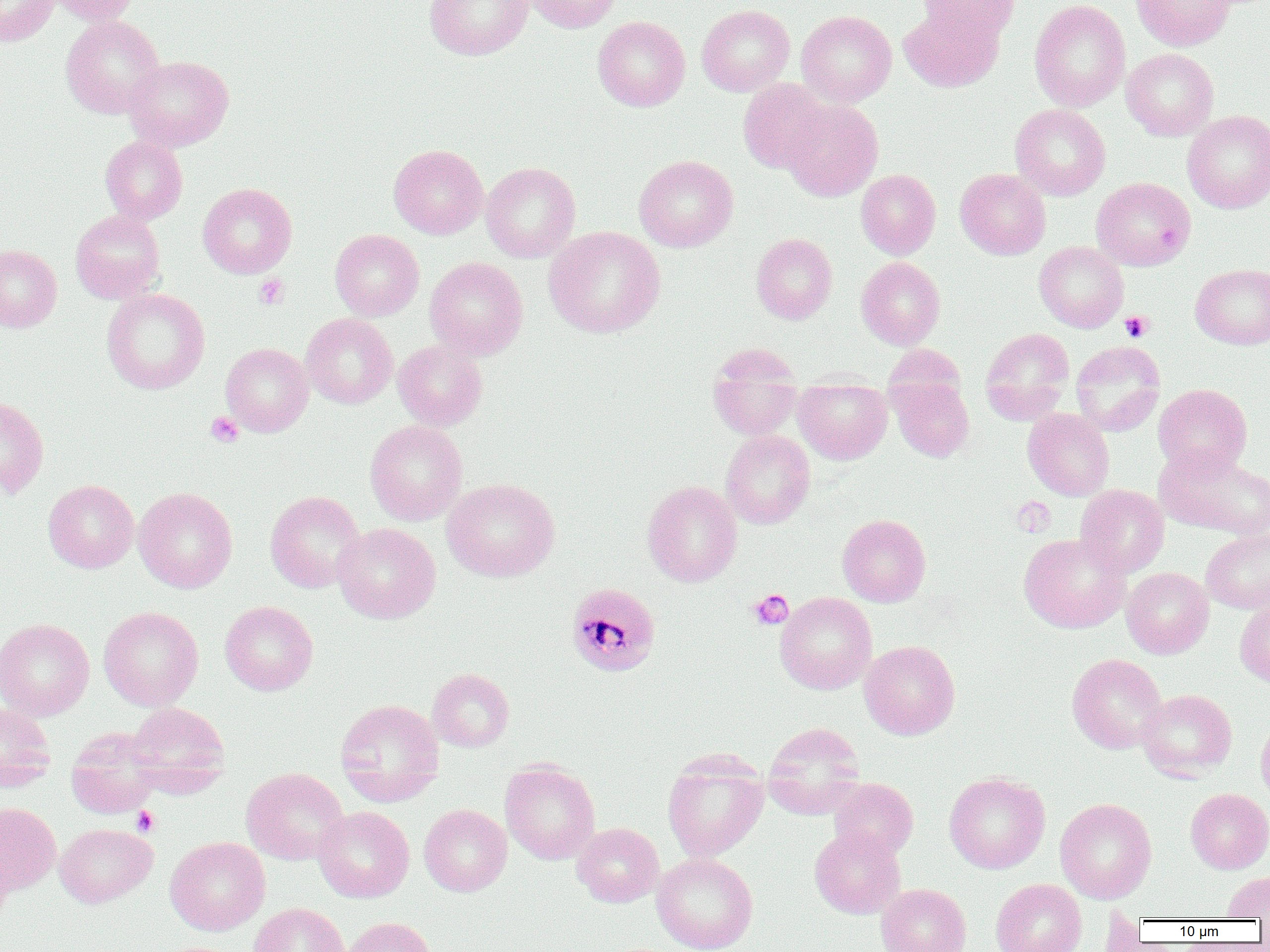

slide_level_diagnosis: Plasmodium malariae
preparation: thin blood smear
platelet_locations: 'approximate bounding boxes as (x1,y1)-(x2,y2) corner pairs in pixels: (254,274)-(289,309), (1120,311)-(1153,342), (205,412)-(244,447), (1012,497)-(1056,536), (748,589)-(794,630), (132,806)-(159,836)'
plasmodium_malariae_infected_red_blood_cell_locations: 'approximate bounding boxes as (x1,y1)-(x2,y2) corner pairs in pixels: (566,583)-(661,677)'
modality: light microscopy
magnification: 1000x
image_size: 1270×952 pixels
uninfected_red_blood_cell_locations: 'approximate bounding boxes as (x1,y1)-(x2,y2) corner pairs in pixels: (0,0)-(58,47), (45,0)-(139,25), (425,0)-(533,60), (524,0)-(622,33), (918,0)-(1021,42), (1029,0)-(1130,112), (1131,0)-(1234,50), (696,4)-(795,96), (898,4)-(1003,92), (797,10)-(896,107), (60,15)-(165,119), (593,16)-(690,111), (1121,48)-(1219,140), (123,56)-(234,151), (738,79)-(831,174), (782,99)-(883,201), (1010,104)-(1110,201), (1182,110)-(1270,213), (100,136)-(188,224), (389,144)-(488,239), (634,155)-(738,252), (480,162)-(580,263), (955,168)-(1051,260), (856,169)-(940,259), (1091,177)-(1195,270), (198,183)-(297,278), (70,210)-(165,303), (544,226)-(665,338), (330,229)-(424,320), (751,232)-(837,325), (1034,241)-(1129,332), (0,245)-(62,332), (425,257)-(528,359), (856,257)-(945,350), (1190,264)-(1270,349), (101,288)-(210,394), (301,313)-(397,409), (980,327)-(1075,425), (392,340)-(488,431), (1070,341)-(1165,435), (221,343)-(314,436), (707,344)-(803,440), (888,376)-(973,462), (794,377)-(892,464), (1154,383)-(1252,475), (0,396)-(49,498), (1023,408)-(1114,500), (365,420)-(467,526), (720,430)-(815,529), (1154,445)-(1266,538), (1202,463)-(1270,539), (442,478)-(560,582), (43,480)-(138,573), (642,480)-(742,587), (1075,484)-(1169,577), (133,487)-(237,593), (265,490)-(366,593), (837,514)-(931,607), (332,522)-(441,623), (1201,530)-(1270,614), (1019,534)-(1131,633), (1121,567)-(1214,658), (775,591)-(877,694), (220,600)-(318,695), (1234,601)-(1270,688), (98,606)-(203,711), (0,618)-(94,720), (860,640)-(960,740), (1067,653)-(1167,754), (427,668)-(515,752), (1136,689)-(1237,780), (335,698)-(444,805), (126,702)-(230,794), (0,703)-(55,789), (1256,716)-(1270,804), (763,722)-(866,818), (66,728)-(163,818), (662,751)-(768,862), (500,761)-(600,864), (241,767)-(349,865), (944,771)-(1050,874), (828,778)-(918,860), (1186,788)-(1270,873), (1055,798)-(1157,903), (0,802)-(60,894), (419,804)-(512,896), (313,805)-(414,903), (572,822)-(664,907), (55,823)-(157,907), (810,828)-(905,918), (165,836)-(270,935), (0,841)-(13,931), (652,853)-(758,952), (1222,871)-(1270,919), (991,878)-(1086,952), (876,883)-(971,952), (248,903)-(349,952), (340,916)-(436,952)'
field_of_view: one of a larger specimen